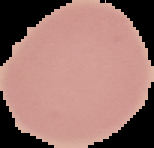
Summary:
  - Result: no Plasmodium parasites detected
  - Image type: cell region segmented out of the field of view; surrounding area masked to black
  - Preparation: thin blood smear
  - Image size: 154×148 pixels